Classify this cell by malaria status.
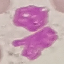
Uninfected.

{
  "stain": "Giemsa",
  "capture": "smartphone camera at the microscope eyepiece",
  "preparation": "thin blood smear",
  "image_type": "automatically extracted cell patch, resized to 64 × 64 pixels"
}